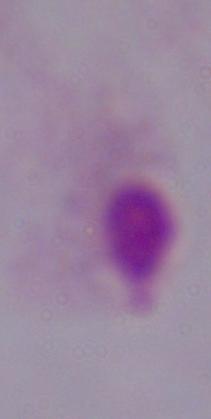

A trichomonad is seen. Photomicrograph. Captured at 1000x magnification.